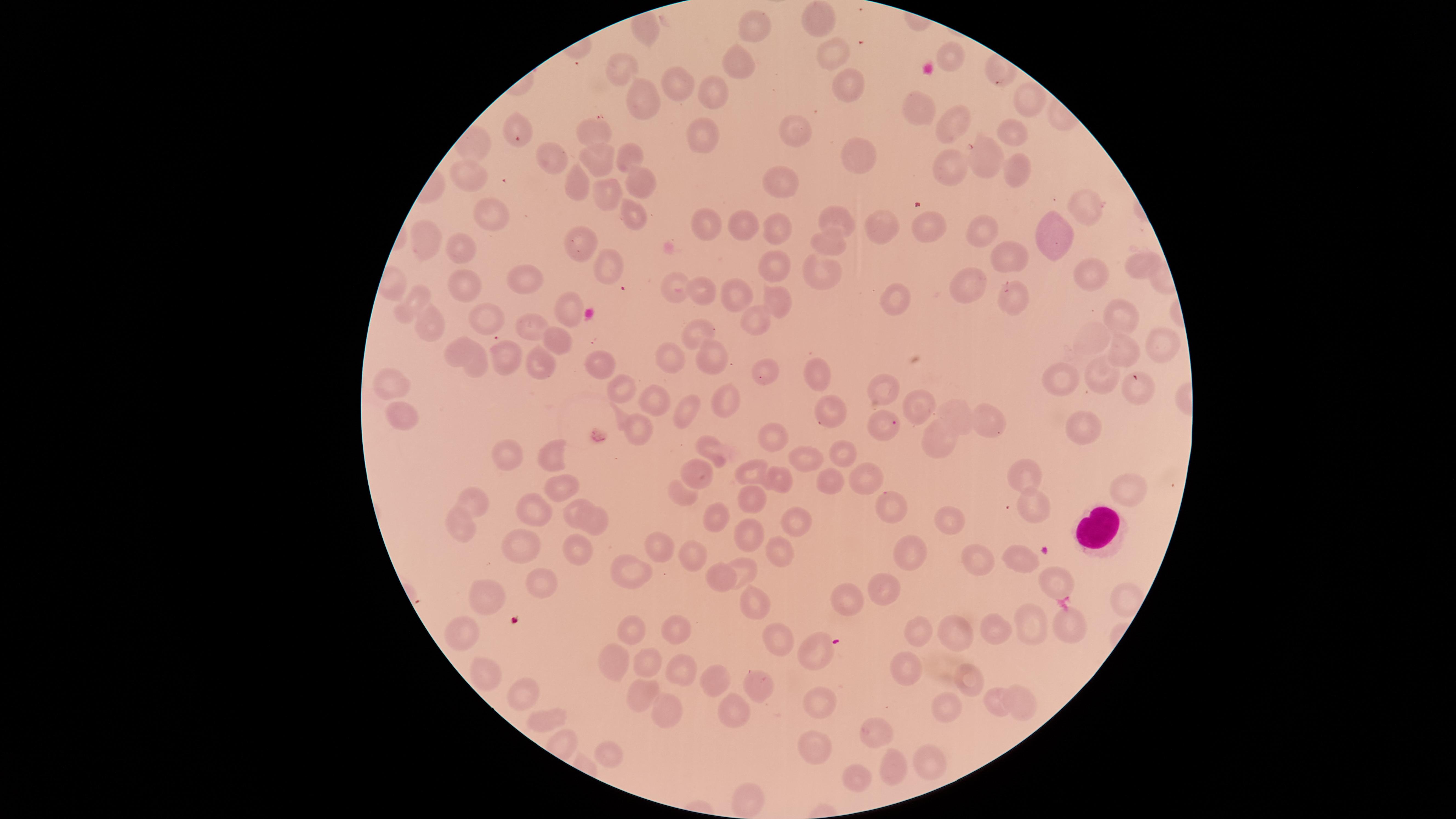
visible region = circular
capture = smartphone photograph through the microscope eyepiece
stain = Giemsa
preparation = thin blood smear
white blood cells = approximate marker points, in pixels from the top-left corner: (x=1096, y=528)
presence = no malaria parasites identified
field of view = single
uninfected red blood cells = approximate marker points, in pixels from the top-left corner: (x=816, y=18), (x=752, y=25), (x=642, y=31), (x=952, y=52), (x=832, y=53), (x=738, y=63), (x=623, y=69), (x=682, y=82), (x=846, y=82), (x=710, y=92), (x=648, y=98), (x=1026, y=105), (x=920, y=109), (x=954, y=119), (x=800, y=128), (x=1012, y=128), (x=519, y=132), (x=701, y=133), (x=596, y=137), (x=628, y=150), (x=981, y=156), (x=862, y=158), (x=557, y=161), (x=597, y=165), (x=946, y=167), (x=1013, y=175), (x=472, y=178), (x=787, y=178), (x=639, y=179), (x=576, y=189), (x=611, y=193), (x=1078, y=208), (x=487, y=212), (x=631, y=215), (x=839, y=217), (x=709, y=221), (x=882, y=221), (x=745, y=225), (x=779, y=227), (x=1053, y=231), (x=930, y=233), (x=978, y=234), (x=584, y=240), (x=831, y=240), (x=434, y=241), (x=461, y=249), (x=1011, y=254), (x=606, y=259), (x=1136, y=264), (x=776, y=269), (x=824, y=272), (x=971, y=277), (x=1086, y=277), (x=524, y=278), (x=461, y=282), (x=677, y=286), (x=701, y=291), (x=736, y=291), (x=1010, y=293), (x=780, y=297), (x=898, y=298), (x=417, y=302), (x=573, y=305), (x=1116, y=319), (x=490, y=321), (x=752, y=322), (x=426, y=326), (x=538, y=328), (x=695, y=331), (x=560, y=336), (x=1156, y=342), (x=1123, y=348), (x=461, y=352), (x=715, y=356), (x=668, y=357), (x=508, y=359), (x=542, y=359), (x=598, y=363), (x=476, y=364), (x=1105, y=371), (x=817, y=374), (x=771, y=375), (x=1063, y=378), (x=398, y=387), (x=1142, y=388), (x=882, y=389), (x=626, y=393), (x=656, y=398), (x=726, y=400), (x=920, y=402), (x=685, y=408), (x=831, y=411), (x=403, y=412), (x=953, y=412), (x=989, y=417), (x=640, y=423), (x=878, y=423), (x=1082, y=427), (x=774, y=435), (x=939, y=439), (x=846, y=449), (x=709, y=453), (x=505, y=456), (x=555, y=458), (x=810, y=458), (x=752, y=472), (x=698, y=473), (x=1030, y=475), (x=781, y=477), (x=865, y=477), (x=558, y=484), (x=828, y=485), (x=1124, y=491), (x=683, y=492), (x=749, y=503), (x=474, y=505), (x=1031, y=508), (x=887, y=509), (x=528, y=514), (x=571, y=514), (x=713, y=522), (x=952, y=523), (x=592, y=524), (x=459, y=528), (x=794, y=529), (x=747, y=536), (x=524, y=547), (x=658, y=551), (x=691, y=552), (x=779, y=552), (x=577, y=554), (x=913, y=555), (x=1024, y=559), (x=974, y=560), (x=740, y=568), (x=629, y=574), (x=718, y=576), (x=1054, y=584), (x=536, y=585), (x=882, y=588), (x=489, y=601), (x=756, y=603), (x=850, y=603), (x=1031, y=621), (x=1067, y=625), (x=679, y=626), (x=465, y=629), (x=990, y=630), (x=957, y=631), (x=920, y=632), (x=631, y=635), (x=777, y=635), (x=812, y=651), (x=621, y=653), (x=648, y=662), (x=681, y=662), (x=906, y=669), (x=483, y=673), (x=715, y=679), (x=971, y=679), (x=757, y=684), (x=524, y=691), (x=644, y=695), (x=1022, y=699), (x=737, y=703), (x=818, y=703), (x=950, y=703), (x=662, y=706), (x=995, y=707), (x=547, y=717), (x=874, y=732), (x=814, y=740), (x=608, y=751), (x=933, y=758), (x=894, y=766), (x=859, y=776)
image size = 1456×819 pixels